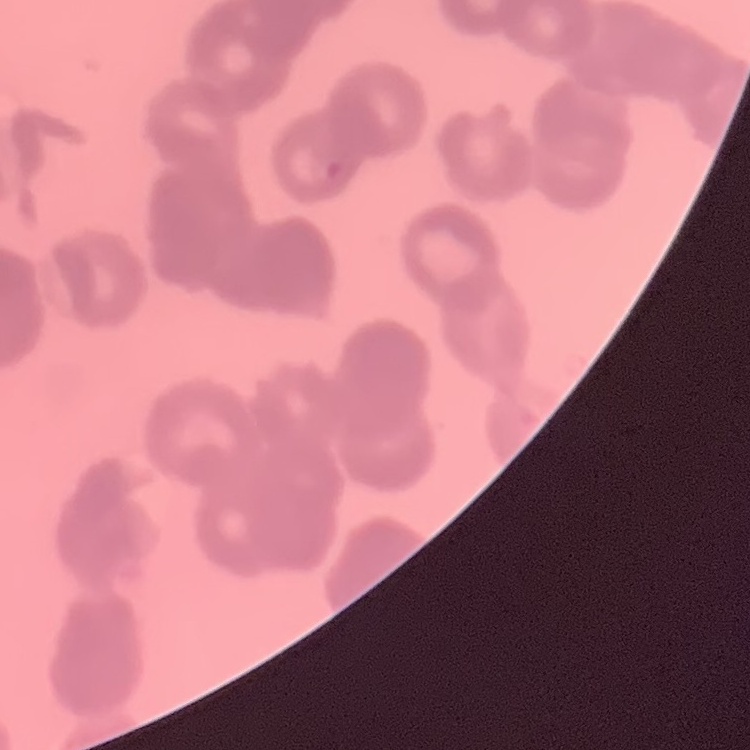
The red blood cells show rouleaux formation. Stained with either Field's or Giemsa. Thin blood smear. Square crop of a larger photomicrograph.